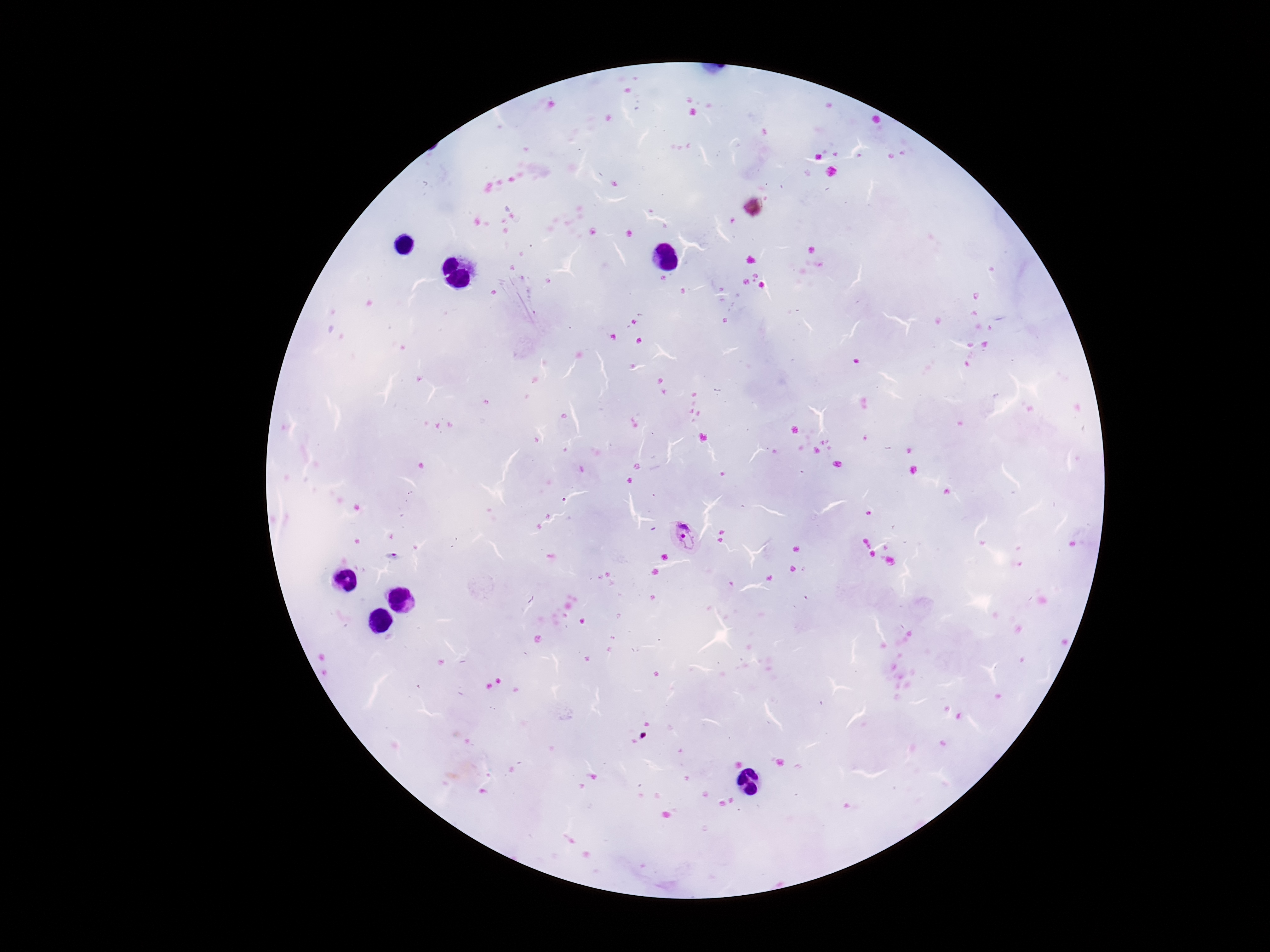
Approximate centers as (x, y) in pixels.
Summary:
  - Plasmodium parasite locations: (685, 540)
  - Capture: smartphone camera through the microscope eyepiece
  - Patient malaria status: infected
  - Stain: Giemsa
  - Preparation: thick peripheral-blood smear
  - Field of view: single
  - Magnification: 100x
  - Image size: 1270×952 pixels